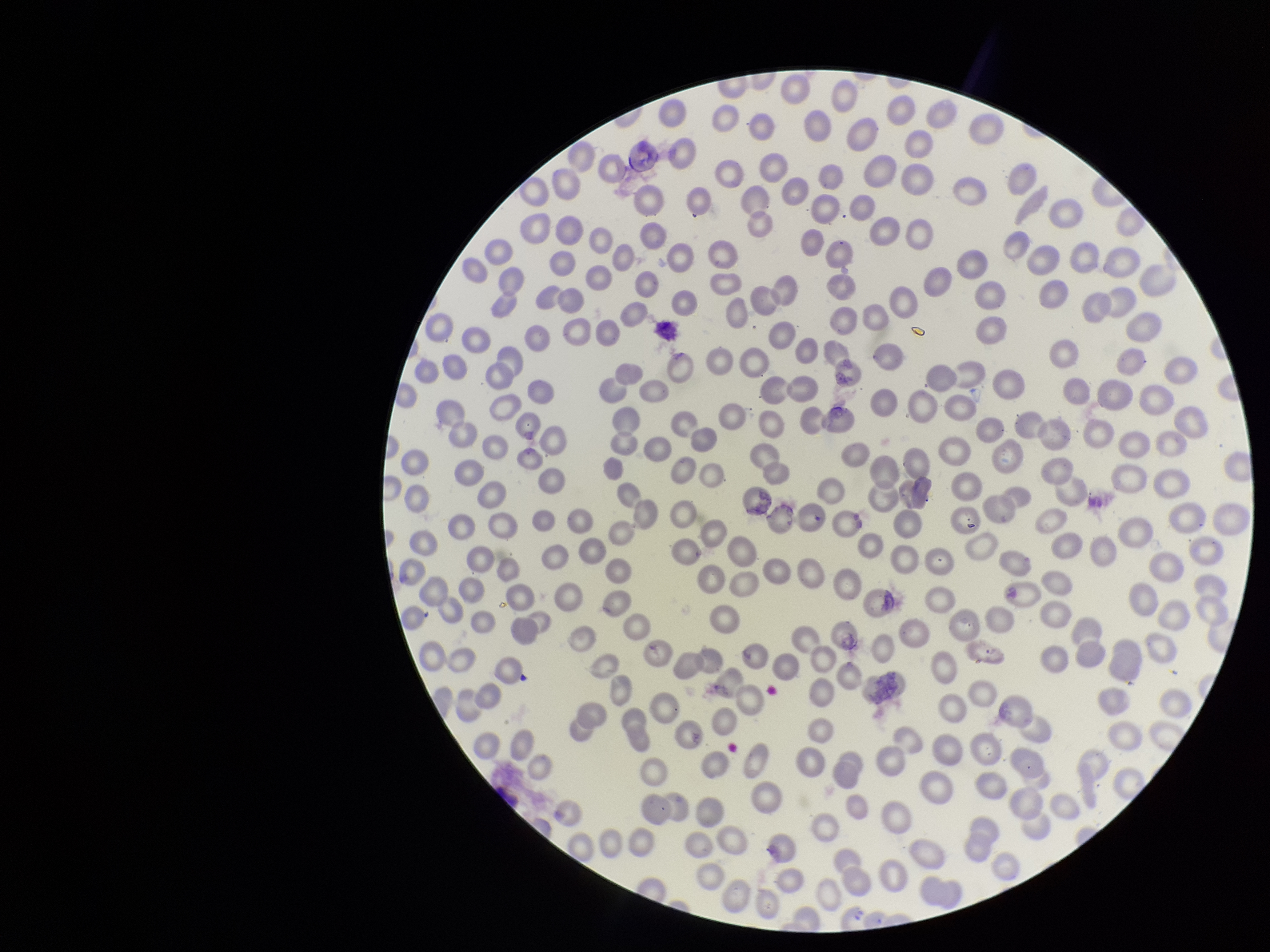

Summary:
  - Parasitized red blood cell count: 0
  - Red blood cell count: 285
  - Stain: Giemsa
  - Parasitized red blood cells: none detected
  - Preparation: thin
  - Patient malaria status: negative
  - Capture: smartphone photograph through the microscope eyepiece
  - Field of view: single
  - Image size: 1270×952 pixels